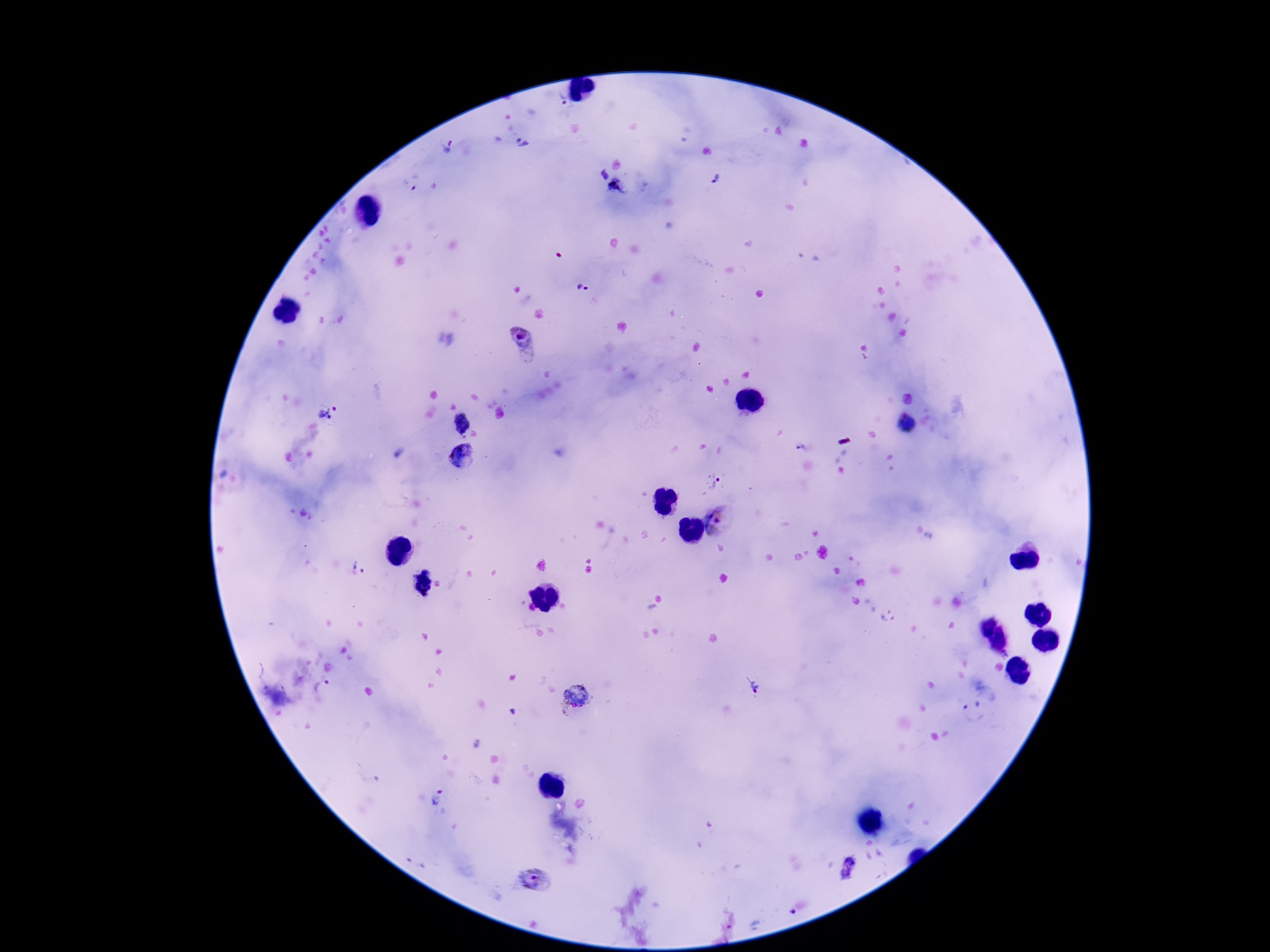

capture = smartphone camera through the microscope eyepiece
Plasmodium parasite locations = approximate centers as (x, y) in pixels: (560, 99), (524, 143), (447, 147), (602, 174), (715, 180), (408, 183), (619, 188), (583, 288), (523, 343), (326, 411), (464, 423), (906, 424), (803, 449), (461, 458), (712, 482), (723, 522), (359, 567), (421, 581), (986, 626), (998, 643), (323, 688), (753, 688), (577, 694), (972, 702), (437, 797), (849, 867), (535, 879), (792, 913)
field of view = one from this slide
magnification = 100x
preparation = thick blood film
stain = Giemsa
patient malaria status = positive
image size = 1270×952 pixels